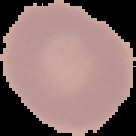
Cell region segmented out of the field of view; the surrounding area is masked to black. Malaria status: uninfected. From a thin blood smear. Image is 136×136 pixels.